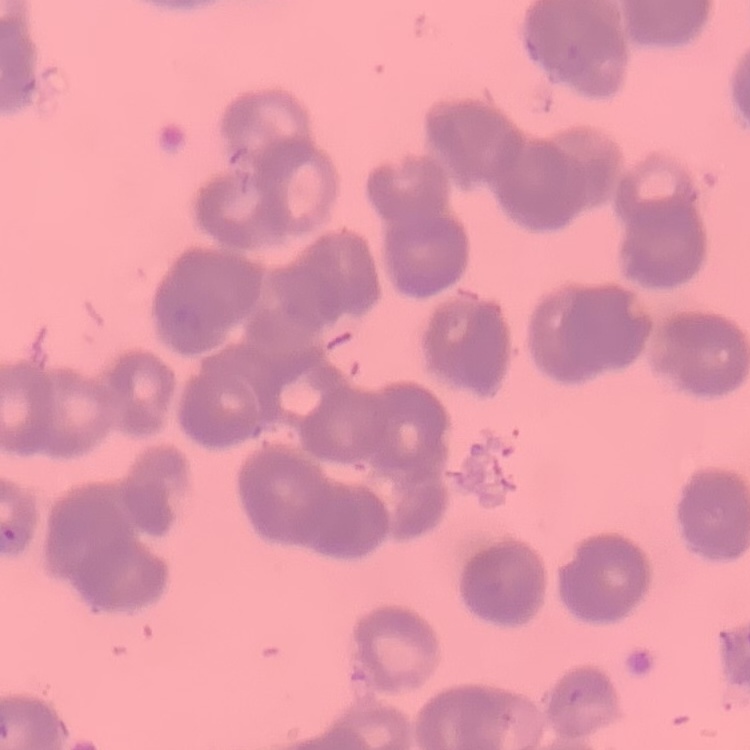
{
  "erythrocyte_morphology": "rouleaux formation",
  "stain": "Field's or Giemsa",
  "image_type": "one tile cut from a larger photomicrograph",
  "preparation": "thin blood film"
}